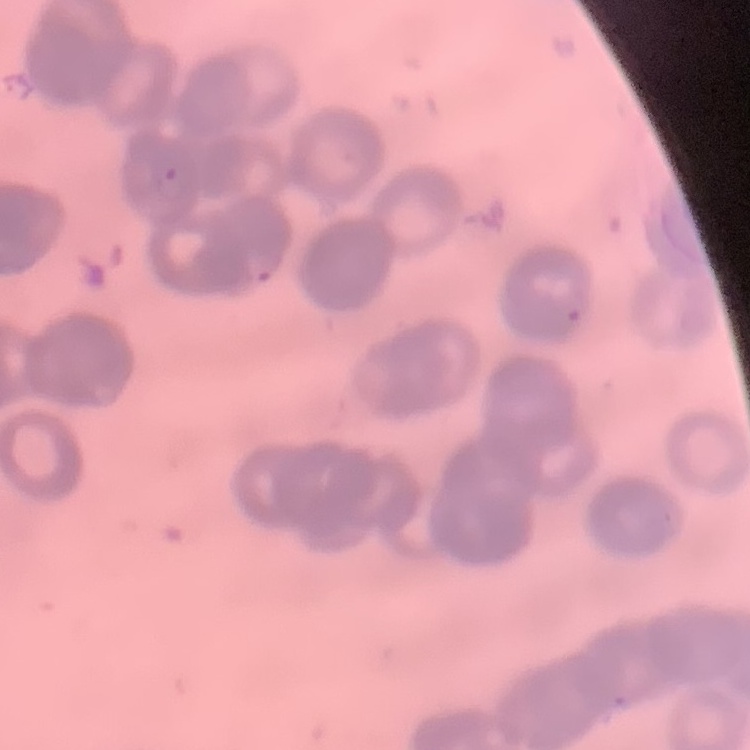 The red blood cells show rouleaux formation. One tile cut from a larger photomicrograph. Field's or Giemsa stain. Thin blood smear.